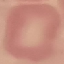

Result: negative for malaria parasites. Thin smear of blood. Giemsa stain. Photographed with a smartphone camera at the microscope eyepiece. Cell patch, automatically extracted from a larger field of view and resized to 64 × 64 pixels.